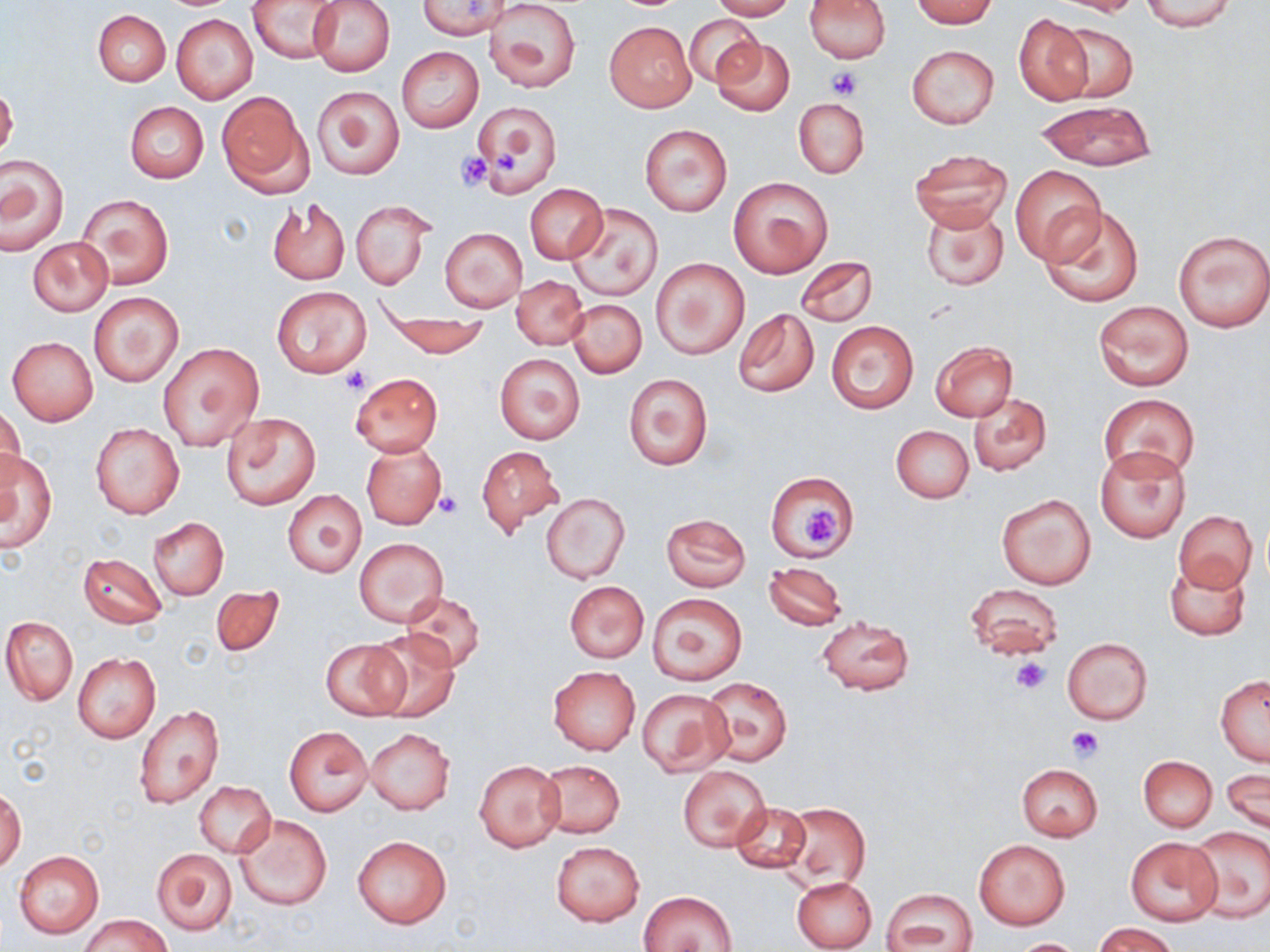

Approximate bounding boxes as [x1, y1, x2, y2] in pixels. Uninfected red blood cell locations: [248, 0, 344, 63], [309, 0, 395, 76], [709, 0, 796, 20], [804, 0, 890, 63], [911, 0, 999, 27], [1052, 0, 1145, 16], [1140, 0, 1238, 32], [418, 1, 505, 38], [485, 1, 582, 94], [93, 9, 170, 87], [171, 14, 258, 104], [684, 14, 763, 87], [1015, 15, 1092, 104], [604, 21, 695, 112], [1057, 22, 1138, 102], [711, 37, 796, 116], [907, 44, 999, 129], [396, 46, 484, 133], [0, 83, 18, 163], [312, 84, 404, 180], [218, 93, 311, 196], [793, 97, 869, 179], [125, 101, 208, 183], [471, 101, 560, 195], [1037, 101, 1155, 170], [639, 123, 733, 216], [908, 149, 1011, 231], [0, 154, 68, 255], [1009, 165, 1106, 264], [729, 176, 833, 278], [525, 183, 607, 265], [77, 194, 173, 290], [266, 195, 351, 285], [351, 199, 431, 290], [920, 202, 1010, 292], [566, 203, 664, 302], [1040, 204, 1144, 308], [439, 227, 527, 312], [1172, 229, 1270, 334], [27, 236, 113, 316], [796, 256, 878, 326], [651, 257, 750, 360], [512, 275, 587, 349], [272, 286, 372, 377], [88, 290, 183, 386], [567, 298, 646, 378], [1094, 301, 1193, 390], [378, 306, 489, 359], [733, 308, 819, 397], [827, 320, 918, 414], [7, 337, 98, 425], [930, 341, 1017, 421], [158, 342, 264, 452], [495, 354, 584, 444], [623, 372, 713, 471], [351, 373, 443, 455], [968, 392, 1051, 475], [1099, 394, 1199, 480], [0, 403, 24, 491], [222, 412, 320, 510], [90, 423, 184, 519], [891, 424, 974, 503], [359, 439, 447, 530], [477, 446, 563, 535], [1096, 446, 1190, 543], [1, 450, 57, 550], [765, 469, 857, 560], [283, 490, 366, 577], [542, 494, 630, 583], [996, 494, 1096, 589], [1173, 510, 1259, 594], [661, 513, 751, 591], [147, 517, 228, 600], [354, 538, 448, 625], [79, 552, 167, 628], [1165, 559, 1250, 640], [763, 563, 847, 630], [564, 581, 648, 662], [965, 583, 1064, 661], [212, 585, 284, 657], [400, 591, 486, 673], [647, 593, 747, 685], [817, 614, 916, 696], [2, 617, 78, 705], [366, 630, 459, 722], [321, 637, 411, 721], [1062, 637, 1152, 724], [72, 652, 160, 743], [548, 666, 639, 754], [700, 675, 791, 767], [1215, 675, 1270, 765], [637, 688, 734, 776], [133, 705, 225, 811], [285, 726, 373, 816], [365, 728, 454, 815], [1139, 756, 1217, 831], [474, 760, 565, 852], [537, 760, 626, 838], [1016, 764, 1103, 841], [677, 766, 771, 852], [1223, 768, 1269, 832], [194, 782, 275, 857], [0, 790, 24, 873], [781, 802, 870, 889], [732, 803, 812, 874], [234, 814, 331, 910], [1186, 826, 1269, 922], [353, 835, 452, 929], [1124, 836, 1224, 927], [974, 839, 1069, 929], [550, 842, 645, 926], [153, 849, 237, 935], [14, 850, 104, 938], [791, 875, 877, 952], [881, 889, 978, 952], [640, 890, 739, 952], [82, 915, 170, 952], [1094, 922, 1178, 952], [1009, 938, 1088, 951]. Platelet locations: [824, 66, 863, 99], [489, 146, 519, 172], [454, 151, 494, 191], [341, 367, 370, 395], [436, 489, 463, 517], [802, 507, 840, 547], [1010, 657, 1050, 694], [1066, 726, 1101, 762]. Slide-level diagnosis: negative for blood parasites. Image is 1270×952 pixels. May-Grünwald-Giemsa stain. Optical microscopy. One field of a larger specimen. Thin blood smear. Captured at 1000x magnification.